State which parasite is depicted.
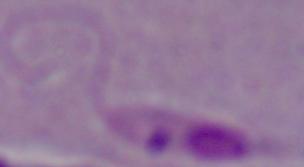

Leishmania.

modality = micrograph
magnification = 1000x